Locate and identify every blood parasite.
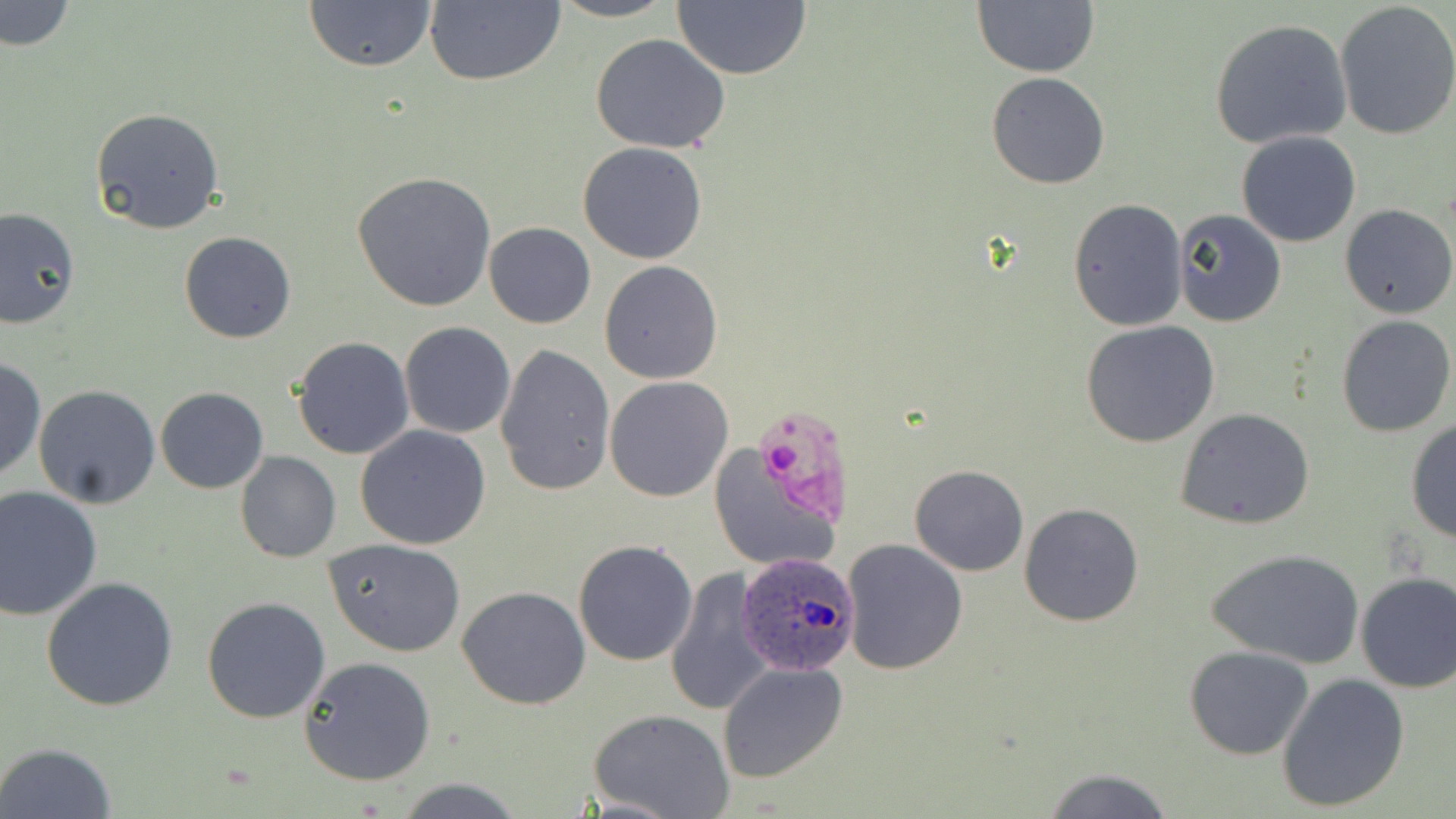
Approximate bounding boxes as (x1, y1, x2, y2) in pixels.
Plasmodium ovale-infected red blood cells: (735, 552, 860, 678).
No Plasmodium falciparum, Plasmodium malariae, Plasmodium vivax, Babesia divergens, or Trypanosoma brucei observed.

Uninfected red blood cell locations: (1, 0, 74, 52), (546, 0, 680, 23), (302, 1, 438, 73), (424, 1, 566, 87), (671, 1, 811, 80), (973, 1, 1099, 77), (1333, 2, 1456, 142), (1208, 18, 1355, 151), (589, 35, 733, 154), (987, 73, 1110, 190), (90, 106, 225, 234), (1236, 131, 1362, 247), (578, 142, 708, 264), (352, 171, 496, 311), (1068, 198, 1187, 330), (1340, 204, 1456, 318), (0, 207, 78, 330), (1172, 209, 1287, 328), (484, 221, 596, 329), (179, 231, 298, 344), (599, 261, 722, 384), (1335, 314, 1455, 438), (1080, 320, 1221, 448), (399, 322, 516, 438), (292, 336, 414, 460), (495, 343, 617, 496), (0, 356, 45, 483), (604, 376, 733, 503), (33, 384, 162, 509), (155, 387, 268, 495), (1175, 408, 1317, 530), (1405, 416, 1456, 545), (356, 425, 492, 550), (706, 443, 843, 573), (235, 451, 340, 562), (909, 465, 1029, 576), (0, 487, 102, 620), (1019, 503, 1144, 627), (324, 538, 466, 657), (841, 538, 968, 674), (572, 539, 698, 667), (1206, 547, 1366, 667), (662, 568, 774, 717), (1353, 571, 1456, 693), (41, 577, 179, 711), (457, 586, 590, 710), (202, 596, 331, 723), (1185, 646, 1314, 760), (299, 656, 436, 785), (718, 662, 850, 784), (1275, 672, 1409, 814), (590, 709, 734, 819), (2, 740, 117, 818), (1040, 766, 1176, 819), (396, 778, 526, 817). Slide-level diagnosis: Plasmodium ovale. Single field of view. May-Grünwald-Giemsa-stained preparation. Thin blood film. Image is 1456×819 pixels. 1000x magnification. Optical microscopy.